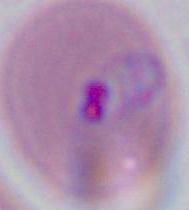 Photomicrograph. 400x or 1000x magnification. A Plasmodium parasite is seen.